Point out each leukocyte.
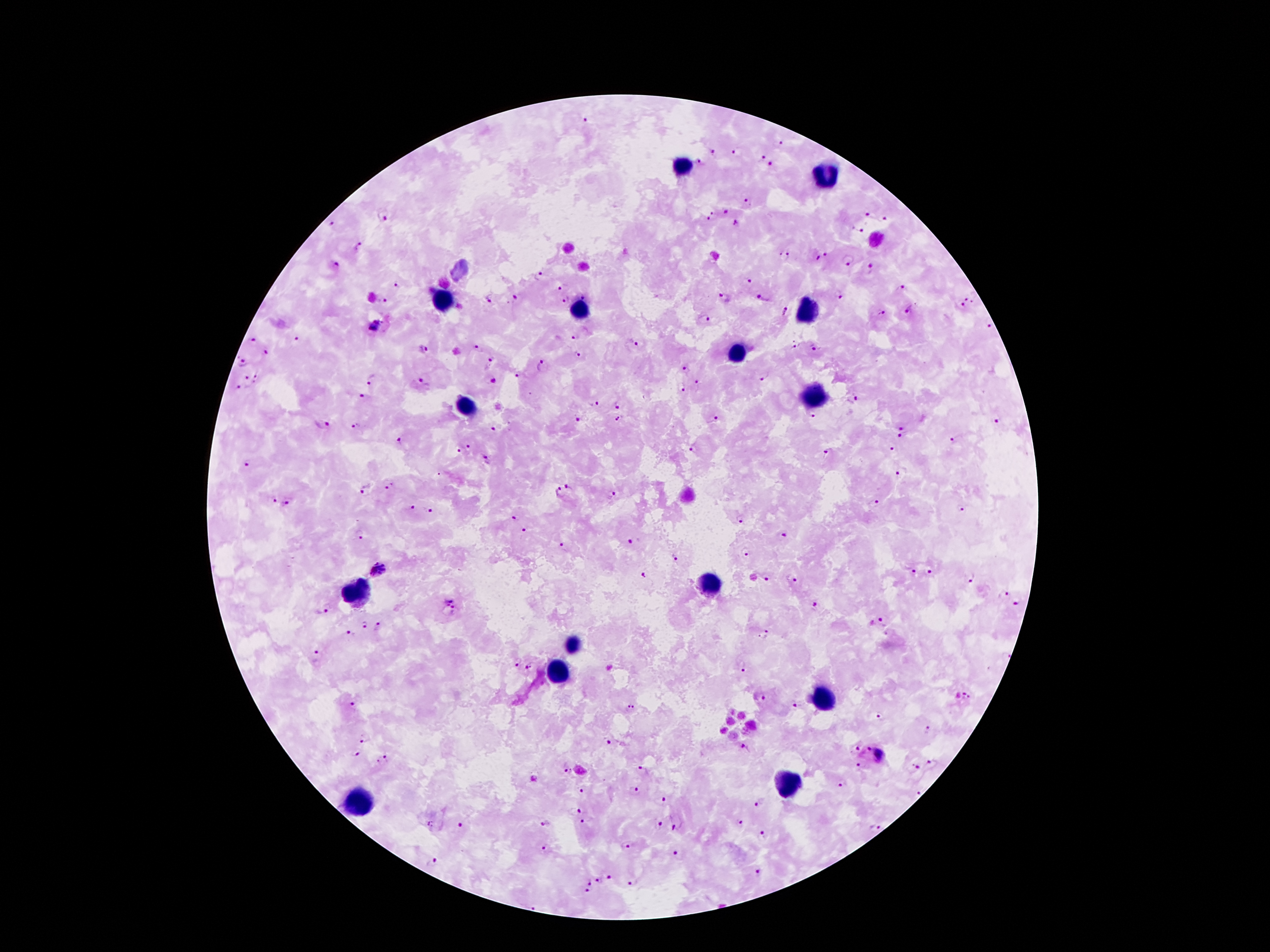

Approximate object centers, in pixels from the top-left corner.
Leukocytes: (x=679, y=166), (x=826, y=176), (x=444, y=301), (x=577, y=311), (x=806, y=313), (x=738, y=354), (x=813, y=398), (x=465, y=405), (x=710, y=584), (x=355, y=593), (x=570, y=645), (x=556, y=670), (x=821, y=695), (x=791, y=782), (x=358, y=805).

Summary:
  - Malaria parasite locations: (x=585, y=120), (x=781, y=143), (x=712, y=152), (x=735, y=153), (x=761, y=158), (x=700, y=163), (x=771, y=166), (x=750, y=202), (x=724, y=212), (x=708, y=215), (x=867, y=215), (x=383, y=217), (x=887, y=221), (x=331, y=223), (x=738, y=223), (x=859, y=230), (x=357, y=247), (x=826, y=253), (x=785, y=256), (x=817, y=258), (x=847, y=261), (x=335, y=263), (x=868, y=269), (x=538, y=276), (x=746, y=280), (x=398, y=284), (x=562, y=287), (x=899, y=287), (x=840, y=295), (x=582, y=297), (x=723, y=298), (x=761, y=298), (x=968, y=298), (x=490, y=299), (x=515, y=299), (x=566, y=299), (x=382, y=300), (x=960, y=307), (x=908, y=311), (x=783, y=313), (x=879, y=314), (x=706, y=318), (x=381, y=320), (x=989, y=326), (x=373, y=328), (x=576, y=337), (x=252, y=340), (x=298, y=341), (x=637, y=345), (x=795, y=345), (x=478, y=348), (x=815, y=348), (x=423, y=349), (x=267, y=352), (x=578, y=356), (x=243, y=362), (x=490, y=362), (x=543, y=364), (x=685, y=368), (x=519, y=375), (x=246, y=376), (x=257, y=376), (x=764, y=378), (x=372, y=379), (x=420, y=381), (x=492, y=382), (x=696, y=383), (x=239, y=388), (x=682, y=388), (x=363, y=395), (x=853, y=400), (x=593, y=405), (x=619, y=405), (x=812, y=415), (x=715, y=418), (x=620, y=419), (x=581, y=420), (x=997, y=421), (x=322, y=425), (x=356, y=425), (x=903, y=428), (x=494, y=429), (x=900, y=437), (x=401, y=440), (x=951, y=440), (x=470, y=446), (x=693, y=448), (x=891, y=450), (x=459, y=452), (x=826, y=454), (x=248, y=463), (x=902, y=473), (x=390, y=486), (x=570, y=487), (x=363, y=490), (x=556, y=494), (x=612, y=495), (x=274, y=501), (x=287, y=502), (x=873, y=504), (x=411, y=507), (x=429, y=510), (x=962, y=510), (x=514, y=518), (x=741, y=520), (x=523, y=530), (x=360, y=536), (x=785, y=536), (x=632, y=542), (x=562, y=544), (x=745, y=552), (x=676, y=557), (x=377, y=570), (x=929, y=571), (x=913, y=572), (x=644, y=574), (x=768, y=577), (x=971, y=579), (x=791, y=581), (x=1004, y=593), (x=452, y=603), (x=1015, y=603), (x=814, y=606), (x=328, y=607), (x=883, y=619), (x=365, y=624), (x=379, y=626), (x=351, y=634), (x=763, y=635), (x=317, y=655), (x=517, y=662), (x=530, y=668), (x=742, y=668), (x=965, y=696), (x=761, y=698), (x=353, y=705), (x=630, y=707), (x=795, y=707), (x=881, y=715), (x=927, y=729), (x=364, y=738), (x=608, y=743), (x=856, y=747), (x=744, y=748), (x=866, y=750), (x=882, y=754), (x=355, y=755), (x=384, y=760), (x=859, y=763), (x=932, y=763), (x=916, y=766), (x=565, y=769), (x=644, y=769), (x=840, y=785), (x=636, y=789), (x=581, y=791), (x=917, y=792), (x=664, y=799), (x=757, y=804), (x=577, y=810), (x=546, y=822), (x=583, y=822), (x=739, y=823), (x=431, y=824), (x=462, y=824), (x=660, y=824), (x=678, y=827), (x=876, y=827), (x=763, y=834), (x=626, y=847), (x=544, y=850), (x=675, y=854), (x=432, y=863), (x=759, y=870), (x=610, y=879), (x=600, y=881), (x=589, y=882), (x=630, y=883), (x=586, y=891), (x=533, y=905)
  - Preparation: thick peripheral-blood smear
  - Capture: smartphone camera through the microscope eyepiece
  - Image size: 1270×952 pixels
  - Field of view: one from this slide
  - Magnification: 100x
  - Patient malaria status: positive for Plasmodium falciparum
  - Stain: Giemsa